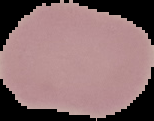

{
  "malaria_status": "uninfected",
  "preparation": "thin blood film",
  "image_size": "154×121 pixels",
  "image_type": "segmented cell region on a black background"
}